Locate and identify every blood parasite.
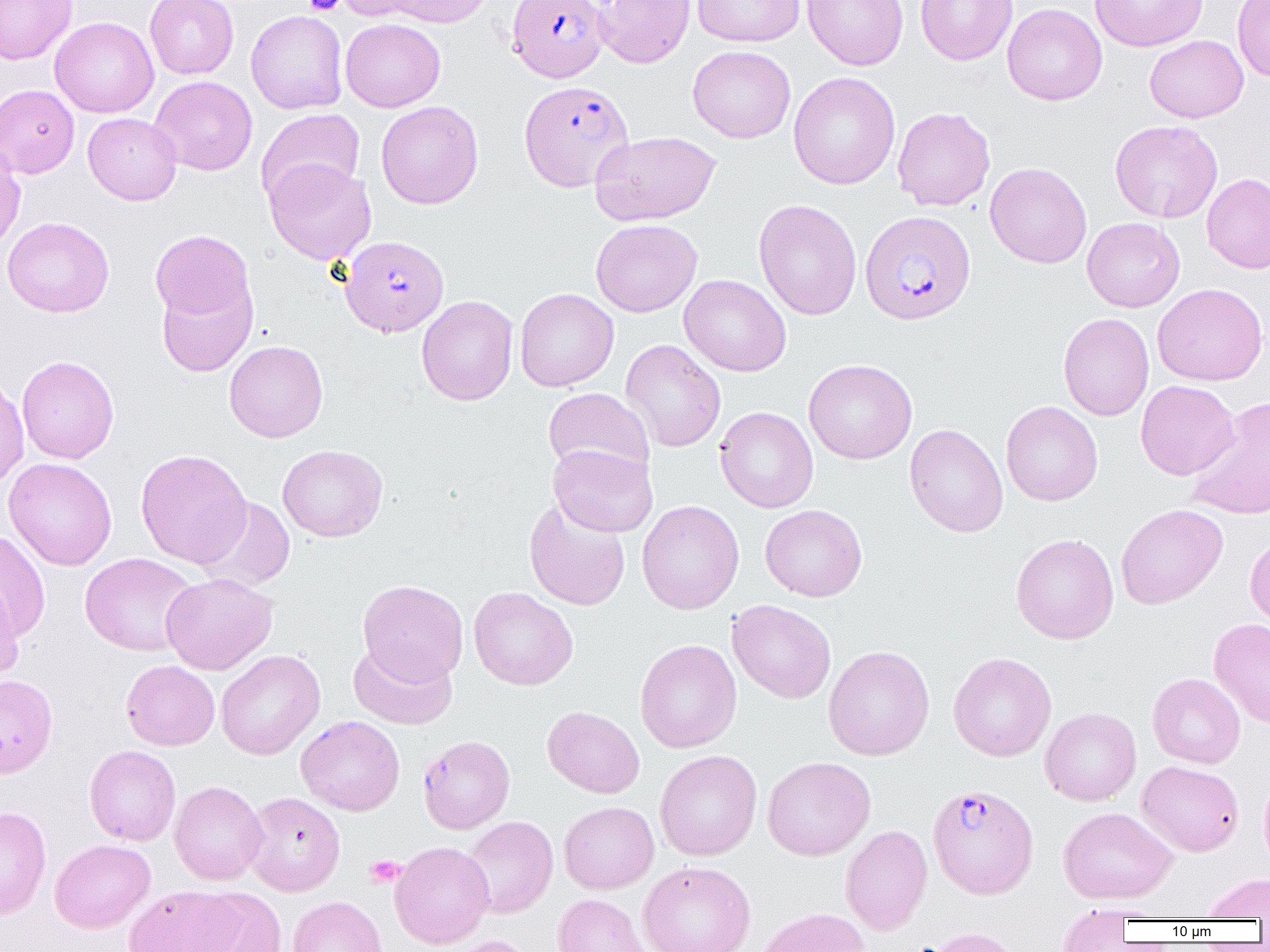

Approximate bounding boxes as (x1,y1)-(x2,y2) corner pairs in pixels.
Plasmodium falciparum-infected red blood cells: (507,0)-(607,82), (518,80)-(634,192), (859,210)-(976,325), (340,236)-(449,338), (417,735)-(515,833), (928,784)-(1038,899).
No Plasmodium ovale, Plasmodium malariae, Plasmodium vivax, Babesia divergens, or Trypanosoma brucei observed.

Uninfected red blood cell locations: (0,0)-(77,64), (145,0)-(238,79), (335,0)-(434,23), (374,0)-(493,27), (592,0)-(695,68), (692,0)-(806,48), (802,0)-(908,70), (915,0)-(1017,65), (1089,0)-(1208,52), (1232,0)-(1270,81), (1002,3)-(1107,106), (246,10)-(348,114), (50,16)-(159,118), (340,18)-(445,112), (1144,35)-(1248,123), (688,45)-(796,143), (788,72)-(900,189), (150,75)-(257,176), (0,84)-(79,178), (376,101)-(484,209), (892,107)-(995,211), (256,108)-(365,208), (83,112)-(182,205), (1109,120)-(1222,223), (590,130)-(721,226), (0,145)-(25,254), (264,158)-(376,265), (985,162)-(1092,268), (1202,173)-(1270,273), (753,198)-(862,320), (2,217)-(114,317), (1082,217)-(1185,312), (591,219)-(702,317), (150,230)-(255,326), (156,274)-(258,377), (679,274)-(791,377), (1152,283)-(1268,385), (515,288)-(618,392), (416,295)-(518,406), (1058,312)-(1154,421), (621,339)-(726,452), (225,340)-(328,442), (16,355)-(119,464), (803,359)-(917,464), (0,375)-(29,490), (1136,380)-(1239,480), (542,387)-(654,482), (1186,396)-(1270,520), (1001,401)-(1103,506), (715,406)-(818,513), (904,424)-(1008,537), (548,443)-(658,537), (277,444)-(388,542), (135,448)-(252,569), (4,457)-(117,570), (196,497)-(295,591), (524,498)-(631,610), (637,500)-(744,614), (1116,503)-(1228,609), (759,504)-(867,601), (0,529)-(51,640), (1010,533)-(1119,644), (1245,535)-(1270,630), (80,553)-(199,656), (161,573)-(277,675), (0,576)-(24,682), (357,579)-(469,684), (468,586)-(578,690), (727,600)-(837,703), (1209,618)-(1270,728), (635,639)-(742,753), (348,640)-(457,729), (823,645)-(935,760), (216,649)-(325,760), (948,652)-(1057,762), (121,660)-(220,751), (1147,673)-(1246,768), (542,706)-(644,798), (1040,707)-(1141,806), (296,715)-(405,816), (84,744)-(181,846), (655,750)-(762,860), (762,756)-(875,861), (1137,760)-(1244,857), (1259,772)-(1270,879), (169,780)-(268,885), (243,791)-(345,896), (559,802)-(659,894), (0,805)-(51,920), (1058,807)-(1177,904), (462,816)-(558,918), (840,825)-(932,935), (50,839)-(155,933), (389,841)-(495,949), (638,861)-(756,952), (1202,873)-(1270,920), (123,885)-(243,952), (190,887)-(288,952), (552,894)-(650,952), (287,896)-(388,952), (755,907)-(870,952), (1056,907)-(1134,951), (919,927)-(1024,952), (440,936)-(538,952). Platelet locations: (303,0)-(343,15), (365,855)-(404,888). Slide-level diagnosis: Plasmodium falciparum. 1000x magnification. One field of a larger specimen. Light microscopy. Image is 1270×952 pixels. Thin blood smear.